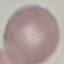

Summary:
  - Malaria status: uninfected
  - Image type: automatically extracted cell patch, resized to 64 × 64 pixels
  - Preparation: thin blood film
  - Stain: Giemsa
  - Capture: smartphone camera at the microscope eyepiece